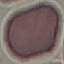 Malaria status: uninfected. Cell patch, automatically extracted from a larger field of view and resized to 64 × 64 pixels. Photographed with a smartphone camera at the microscope eyepiece. Giemsa stain. Thin blood smear.